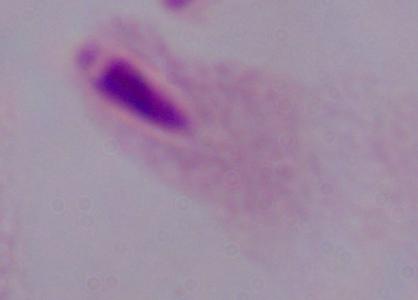
Summary:
  - Identification: trichomonad
  - Modality: micrograph
  - Magnification: 1000x